Assess this cell for malaria.
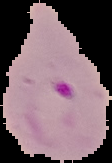

It is parasitized.

Summary:
  - Preparation: thin blood smear
  - Image size: 112×163 pixels
  - Image type: segmented cell region with the area outside set to black